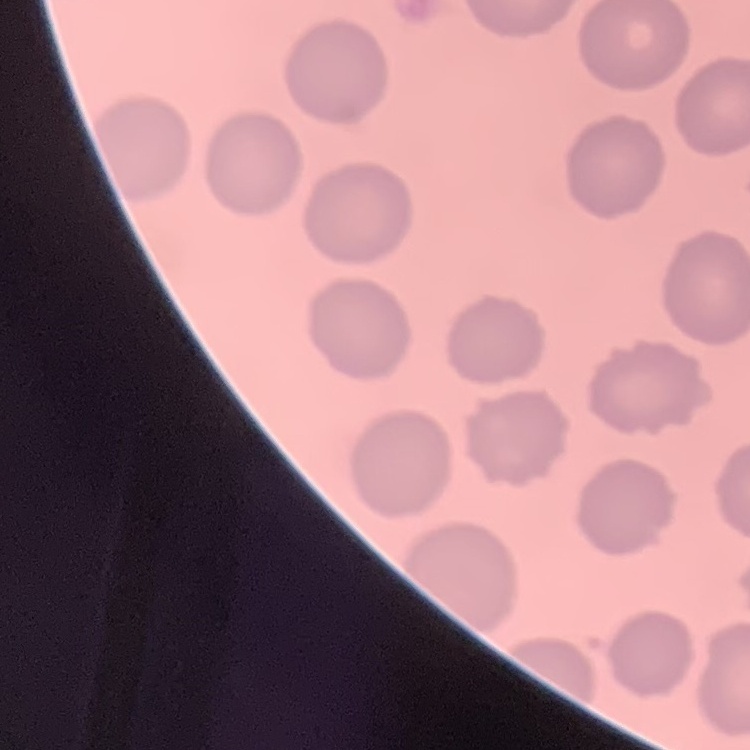 The erythrocytes exhibit no rouleaux formation. Stained with either Field's or Giemsa. Square crop of a larger photomicrograph. Thin peripheral smear.